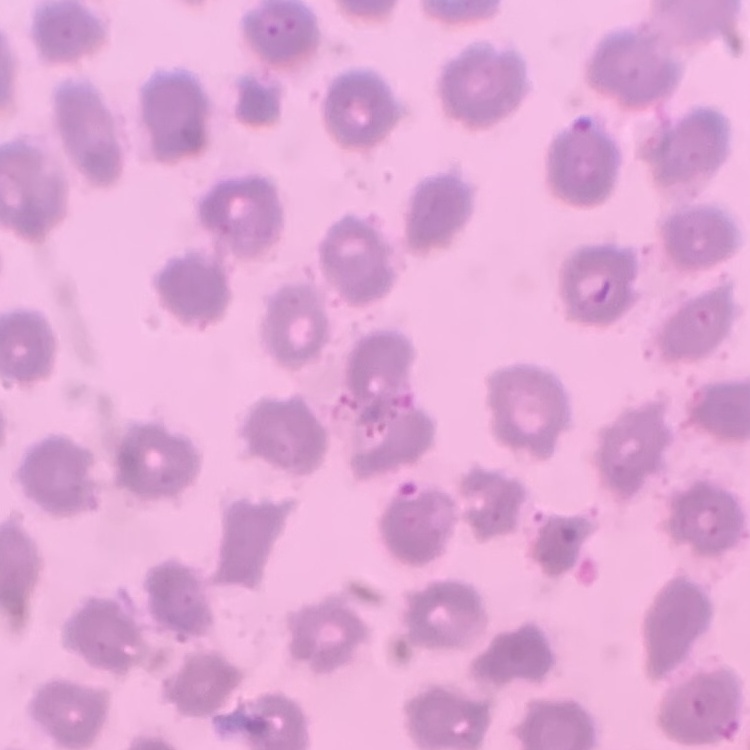

Summary:
  - Red blood cell morphology: no rouleaux formation
  - Image type: one tile cut from a larger photomicrograph
  - Stain: Field's or Giemsa
  - Preparation: thin blood smear